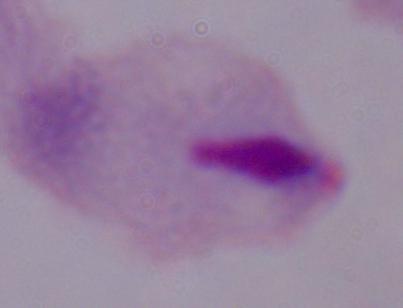
Summary:
  - Identification: trichomonad
  - Magnification: 1000x
  - Modality: micrograph